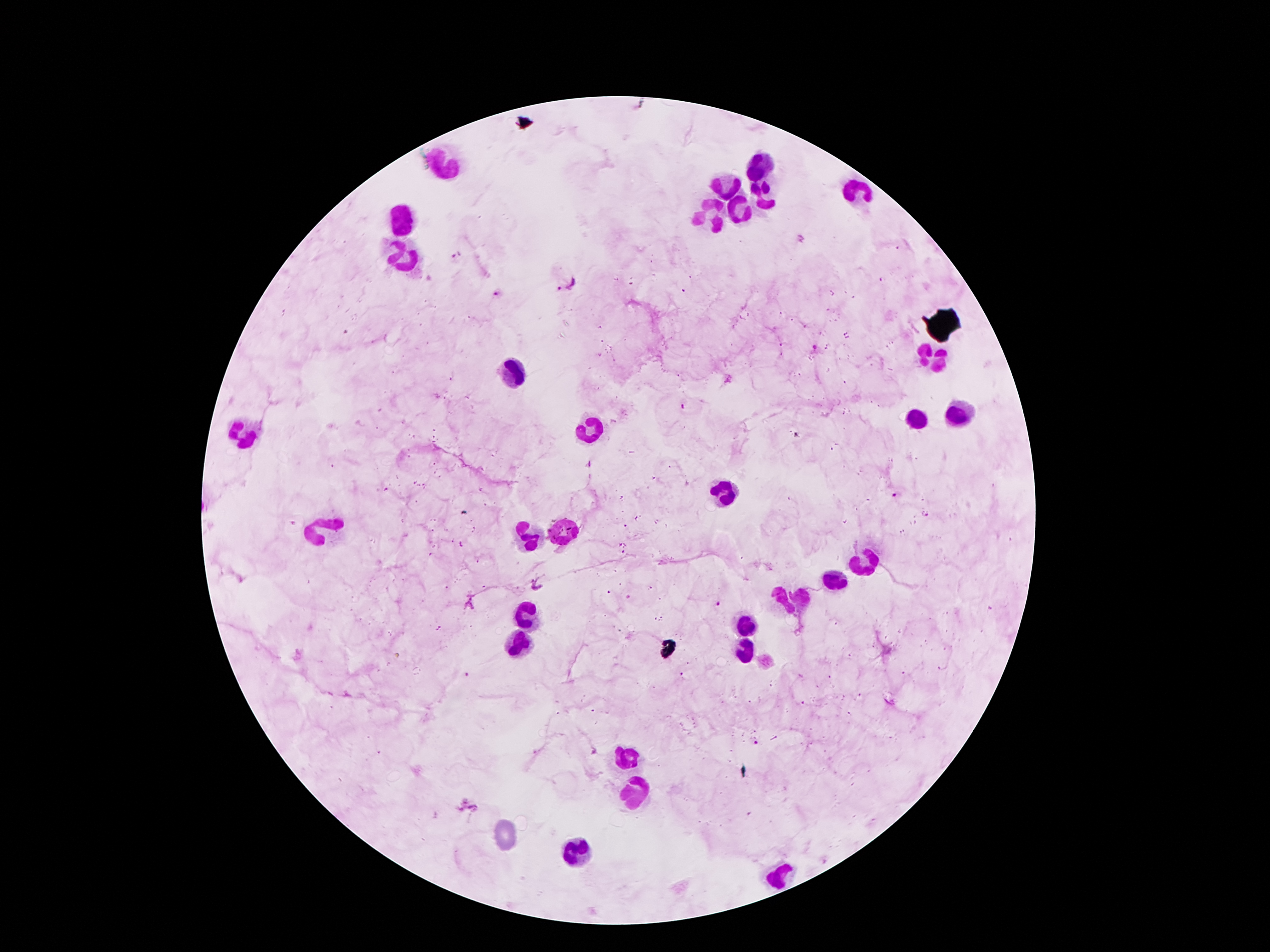
Approximate centers as (x, y) in pixels.
Summary:
  - Leukocyte locations: (444, 163), (761, 163), (730, 186), (764, 193), (857, 193), (743, 209), (711, 211), (401, 220), (400, 263), (932, 359), (512, 375), (961, 414), (916, 418), (591, 430), (250, 436), (723, 488), (325, 529), (566, 530), (527, 536), (864, 561), (832, 575), (796, 602), (528, 616), (748, 622), (514, 643), (741, 648), (625, 756), (632, 795), (580, 852), (779, 873)
  - Malaria parasite locations: (457, 256), (566, 284), (496, 294), (816, 347), (728, 380), (682, 406), (894, 494), (925, 515), (717, 603), (468, 675), (756, 743), (466, 807)
  - Field of view: single
  - Capture: smartphone camera through the microscope eyepiece
  - Image size: 1270×952 pixels
  - Preparation: thick peripheral-blood smear
  - Stain: Giemsa
  - Magnification: 100x
  - Patient malaria status: infected with Plasmodium falciparum